Locate and identify every blood parasite.
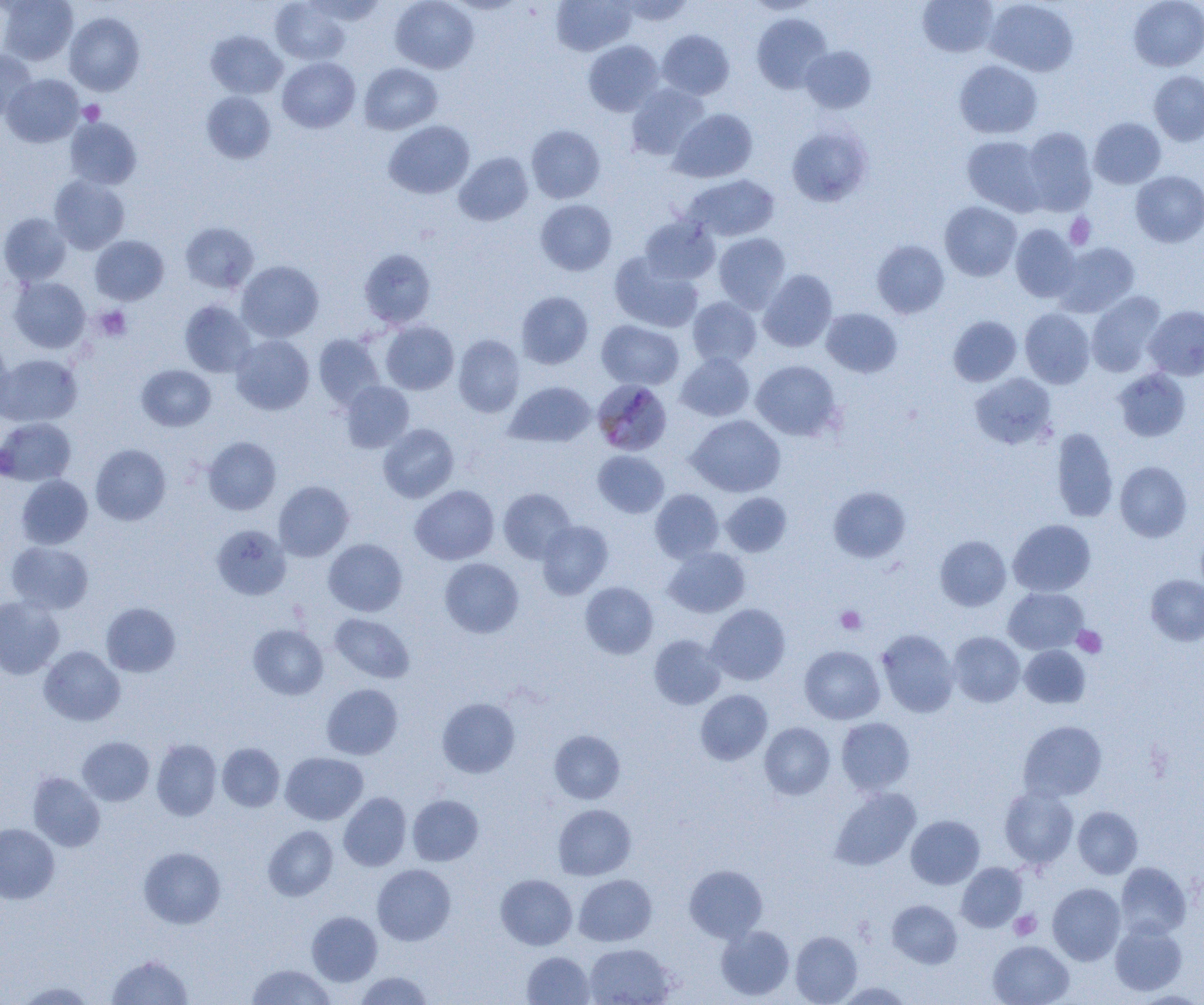

Approximate bounding boxes as (x1, y1, x2, y2) in pixels.
Plasmodium malariae-infected red blood cells: (595, 380, 675, 456).
No Plasmodium falciparum, Plasmodium ovale, Plasmodium vivax, Babesia divergens, or Trypanosoma brucei observed.

slide_level_diagnosis: Plasmodium malariae
magnification: 1000x
uninfected_red_blood_cell_locations: 'approximate bounding boxes as (x1, y1, x2, y2) in pixels: (0, 0, 78, 66), (271, 0, 350, 65), (305, 0, 388, 24), (390, 0, 479, 73), (552, 0, 636, 55), (617, 0, 693, 26), (745, 0, 823, 15), (917, 0, 998, 57), (984, 0, 1078, 76), (1129, 0, 1204, 71), (64, 12, 144, 96), (752, 13, 832, 93), (206, 30, 286, 99), (657, 30, 734, 99), (583, 40, 664, 116), (800, 46, 876, 114), (0, 50, 36, 120), (277, 57, 360, 132), (954, 60, 1042, 139), (359, 63, 442, 134), (1149, 71, 1204, 145), (2, 74, 84, 147), (626, 83, 710, 160), (202, 91, 275, 164), (669, 109, 757, 182), (65, 117, 141, 189), (1089, 117, 1166, 188), (383, 120, 474, 199), (786, 124, 873, 207), (526, 125, 605, 203), (1021, 127, 1097, 215), (962, 136, 1047, 215), (454, 152, 533, 226), (1131, 171, 1204, 247), (683, 174, 779, 242), (49, 175, 130, 254), (535, 199, 617, 276), (939, 201, 1022, 281), (0, 213, 72, 286), (639, 215, 720, 284), (180, 222, 259, 293), (1010, 224, 1080, 302), (713, 233, 791, 313), (90, 235, 169, 305), (871, 240, 950, 318), (1055, 242, 1139, 317), (359, 248, 436, 329), (609, 252, 703, 332), (236, 260, 324, 342), (758, 269, 837, 352), (9, 276, 90, 353), (516, 291, 593, 369), (1086, 291, 1166, 377), (687, 296, 762, 368), (179, 300, 256, 377), (1145, 305, 1204, 380), (821, 308, 902, 377), (1019, 308, 1095, 389), (948, 316, 1022, 386), (597, 320, 684, 390), (381, 321, 459, 394), (313, 334, 385, 410), (0, 335, 11, 414), (231, 335, 314, 415), (453, 335, 525, 417), (676, 353, 755, 421), (0, 354, 82, 427), (750, 360, 842, 441), (137, 364, 216, 431), (1113, 368, 1191, 442), (970, 373, 1057, 449), (340, 381, 414, 453), (505, 381, 596, 447), (687, 414, 785, 497), (0, 418, 76, 486), (378, 423, 459, 503), (1051, 427, 1119, 523), (203, 437, 281, 515), (90, 444, 171, 525), (592, 450, 669, 518), (1115, 461, 1192, 542), (16, 475, 92, 549), (273, 481, 354, 561), (410, 485, 499, 565), (829, 486, 910, 563), (498, 487, 576, 563), (650, 489, 724, 563), (721, 492, 792, 557), (1008, 519, 1095, 596), (537, 520, 613, 599), (211, 524, 291, 600), (935, 535, 1011, 611), (323, 539, 407, 616), (6, 541, 93, 614), (664, 546, 750, 618), (439, 557, 524, 638), (1145, 575, 1204, 646), (581, 582, 658, 659), (1003, 587, 1088, 654), (0, 595, 65, 679), (101, 602, 181, 677), (705, 604, 790, 685), (329, 613, 414, 683), (248, 624, 328, 699), (877, 629, 959, 717), (948, 632, 1025, 707), (649, 635, 726, 709), (799, 645, 885, 724), (1020, 645, 1090, 707), (39, 646, 125, 725), (321, 683, 403, 759), (695, 689, 772, 765), (437, 697, 520, 778), (836, 717, 915, 796), (1018, 720, 1107, 801), (759, 722, 835, 799), (549, 730, 625, 804), (77, 736, 154, 805), (152, 739, 221, 820), (217, 743, 284, 811), (281, 752, 368, 825), (28, 772, 105, 852), (999, 786, 1079, 869), (830, 787, 921, 870), (339, 792, 411, 871), (407, 794, 484, 866), (553, 803, 636, 880), (1073, 806, 1142, 879), (906, 815, 985, 889), (0, 823, 60, 903), (263, 826, 338, 901), (139, 847, 225, 928), (956, 862, 1027, 932), (1115, 862, 1191, 939), (372, 864, 456, 945), (685, 864, 767, 942), (495, 874, 577, 950), (574, 874, 656, 946), (1048, 882, 1125, 965), (887, 899, 962, 968), (306, 911, 382, 986), (1110, 922, 1187, 995), (716, 925, 795, 1000), (790, 931, 862, 1004), (988, 940, 1074, 1005), (584, 943, 675, 1005), (522, 951, 594, 1005), (107, 955, 193, 1004), (247, 964, 336, 1005), (353, 971, 433, 1004), (15, 981, 96, 1004), (833, 981, 914, 1004)'
field_of_view: one of a larger specimen
platelet_locations: 'approximate bounding boxes as (x1, y1, x2, y2) in pixels: (78, 100, 105, 125), (1065, 213, 1096, 249), (95, 305, 132, 341), (835, 606, 866, 634), (1072, 626, 1107, 658), (1009, 910, 1041, 940)'
modality: light microscopy
image_size: 1204×1005 pixels
preparation: thin blood film